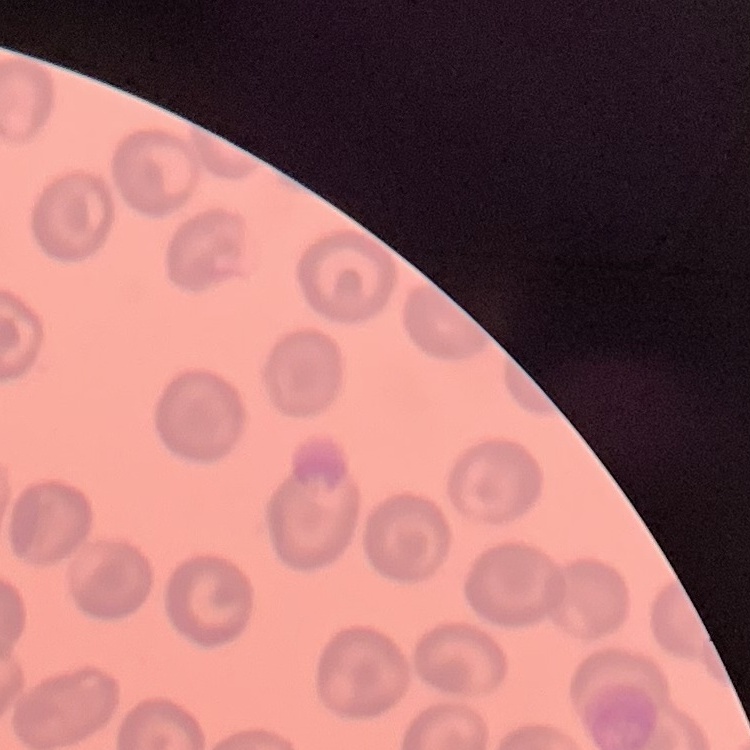 The red blood cells exhibit no rouleaux formation. Field's or Giemsa stain. One tile cut from a larger photomicrograph. Thin blood film.